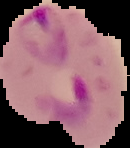

From a thin blood smear. Malaria status: parasitized. Image is 130×148 pixels. Cell region segmented out of the field of view; the surrounding area is masked to black.